Classify this cell by malaria status.
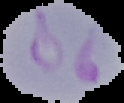

It is parasitized.

Summary:
  - Image size: 124×103 pixels
  - Image type: segmented cell region with the area outside set to black
  - Preparation: thin blood smear